State the preparation type.
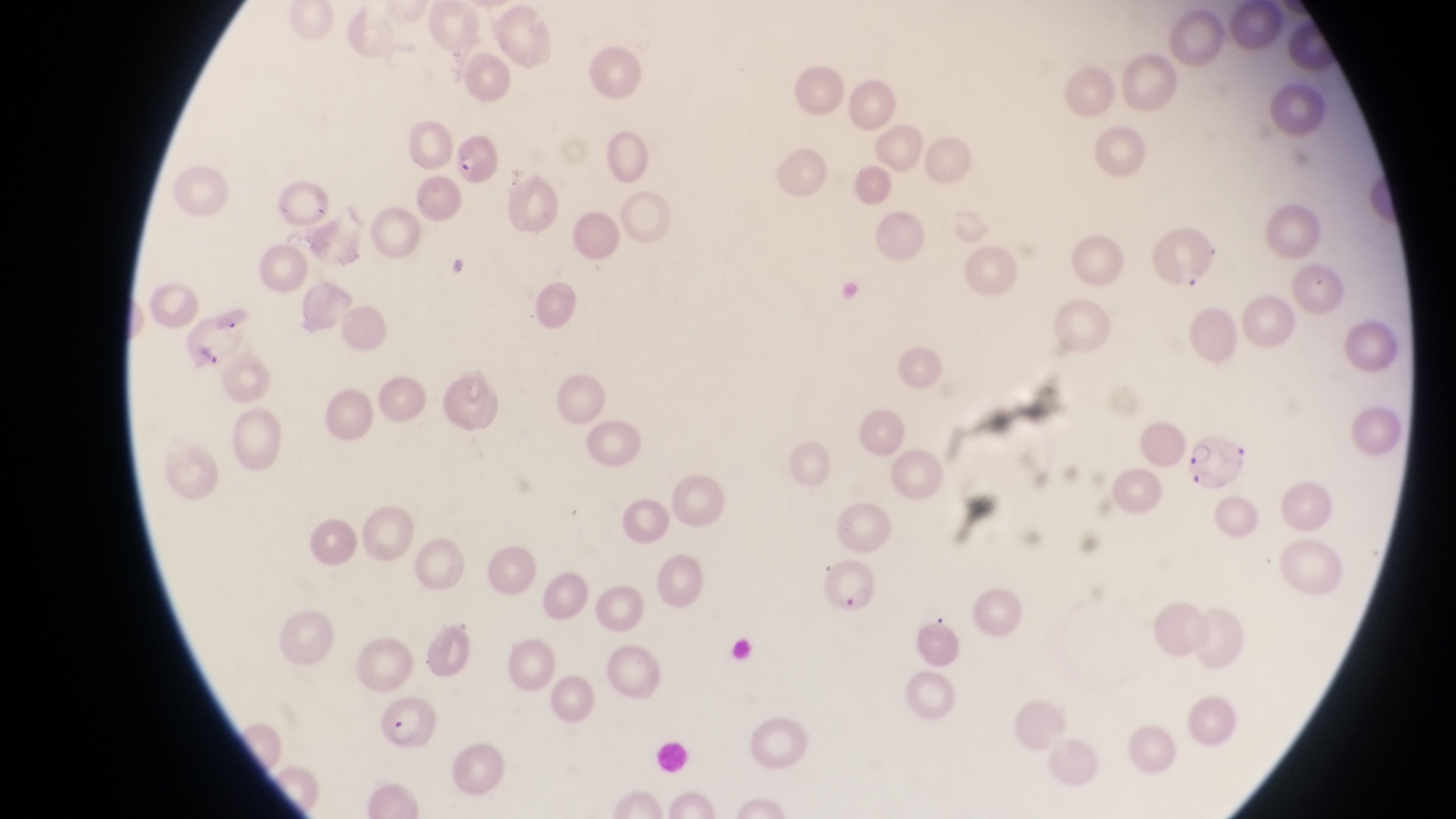
This is a thin smear.

Approximate bounding boxes as {left, top, right, bottom} in pixels. Parasitised red blood cell locations: {449, 129, 502, 189}, {1186, 429, 1249, 490}, {817, 551, 875, 614}, {375, 695, 436, 747}. Magnification of 1000x. Image is 1456×819 pixels. Photographed through the eyepiece of an Olympus CX-23 microscope with a smartphone camera. Single field of view. Collected in Uganda.